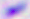

magnification = 400x
modality = micrograph
identification = Toxoplasma gondii